Locate and identify every blood parasite.
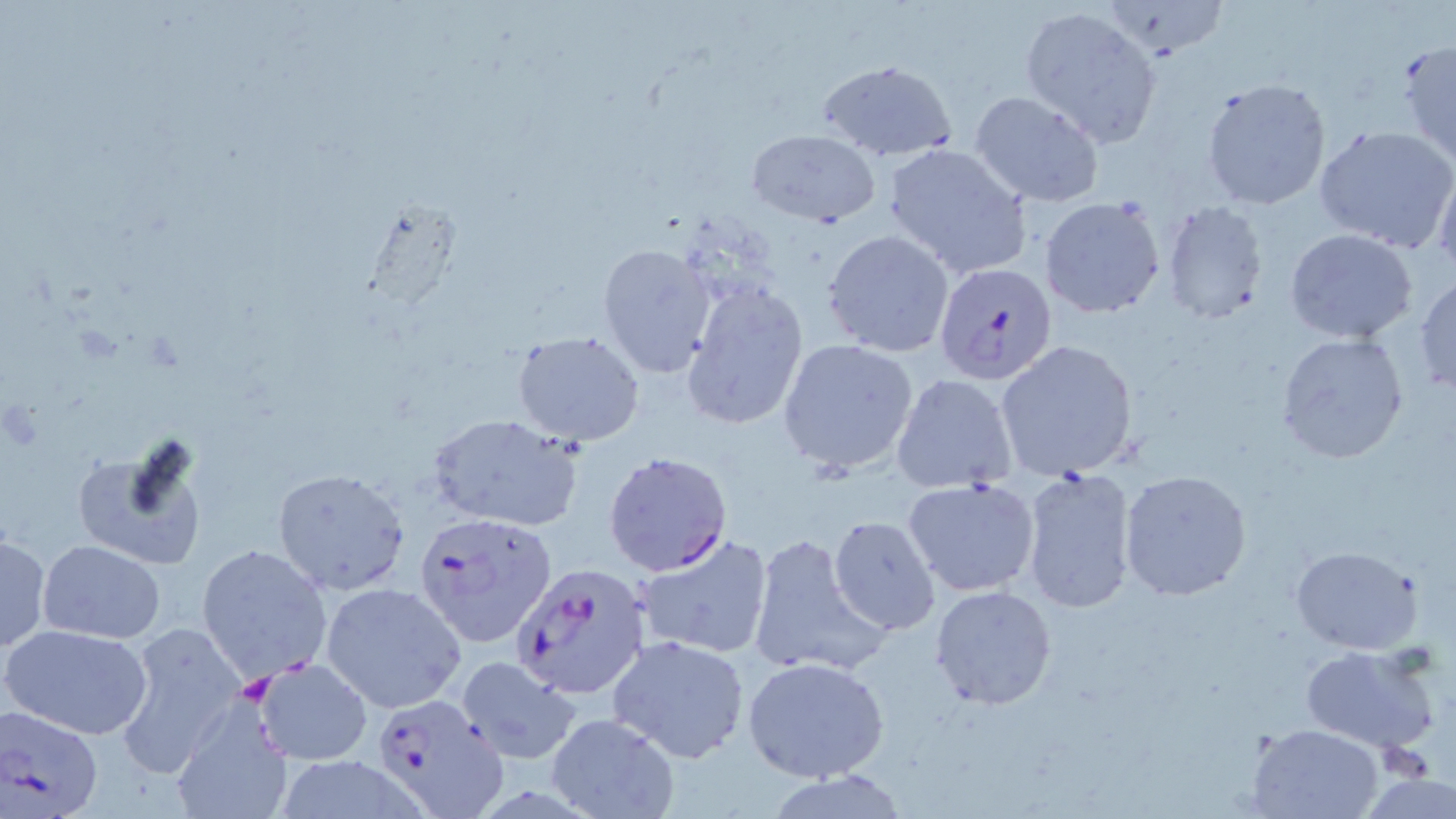
Approximate bounding boxes as (x1,y1)-(x2,y2) corner pairs in pixels.
Plasmodium falciparum-infected red blood cells: (933,262)-(1058,385), (602,451)-(733,576), (415,511)-(559,650), (507,563)-(646,697), (367,690)-(509,815), (2,704)-(105,819).
No Plasmodium ovale, Plasmodium malariae, Plasmodium vivax, Babesia divergens, or Trypanosoma brucei observed.

slide-level diagnosis = Plasmodium falciparum
field of view = single
stain = May-Grünwald-Giemsa
preparation = thin blood film
image size = 1456×819 pixels
platelet locations = approximate bounding boxes as (x1,y1)-(x2,y2) corner pairs in pixels: (237,674)-(276,705)
uninfected red blood cell locations = approximate bounding boxes as (x1,y1)-(x2,y2) corner pairs in pixels: (1018,5)-(1166,148), (1396,39)-(1456,167), (815,59)-(957,162), (1199,77)-(1332,211), (970,90)-(1105,207), (1315,124)-(1455,252), (747,128)-(878,226), (884,144)-(1033,278), (1434,163)-(1456,280), (1040,197)-(1166,317), (1159,202)-(1269,323), (1283,228)-(1420,345), (824,229)-(955,358), (598,242)-(717,378), (1414,272)-(1456,396), (680,279)-(809,432), (512,331)-(646,447), (1274,332)-(1410,465), (776,338)-(920,474), (994,340)-(1141,483), (890,373)-(1018,494), (427,412)-(584,531), (70,434)-(211,573), (1018,465)-(1138,613), (271,467)-(410,597), (1119,469)-(1253,600), (903,477)-(1042,597), (828,516)-(941,636), (747,532)-(889,679), (634,533)-(776,661), (0,534)-(50,653), (38,539)-(164,642), (196,542)-(332,683), (1288,545)-(1426,655), (319,582)-(466,714), (930,585)-(1058,711), (114,620)-(248,776), (1,622)-(154,740), (606,634)-(751,764), (1298,644)-(1442,754), (455,654)-(583,765), (743,656)-(890,783), (251,657)-(375,765), (168,695)-(292,819), (545,713)-(679,819), (1245,722)-(1388,819)
modality = optical microscopy
magnification = 1000x